Point out each Plasmodium parasite.
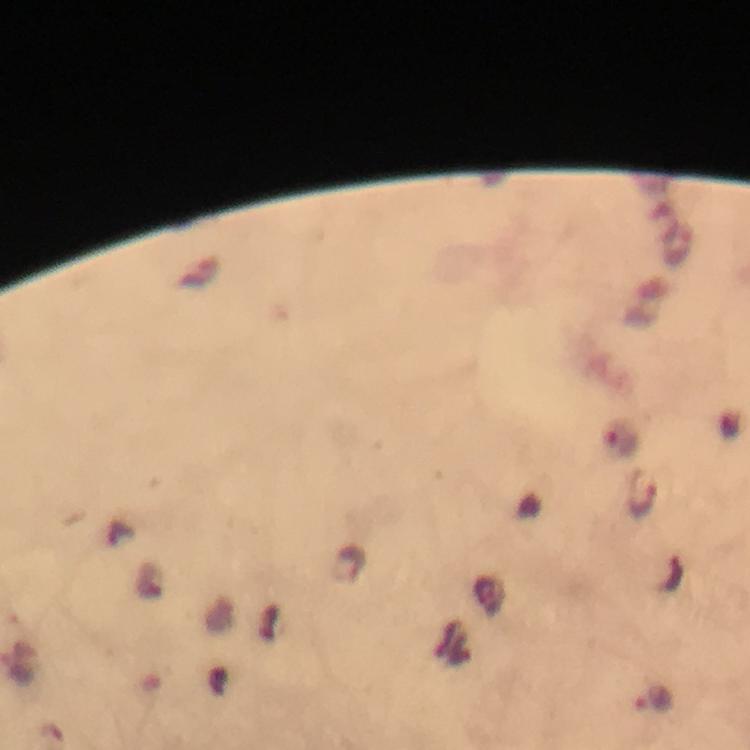

Approximate centers as {x, y} in pixels.
Plasmodium parasites: {643, 494}, {348, 564}, {655, 700}.

Giemsa-stained preparation. Smartphone photograph taken through a microscope. Cropped region of a single field of view. Immersion oil applied. Thick blood film. From a malaria diagnostic workup. At 100x magnification. Image is 750×750 pixels.